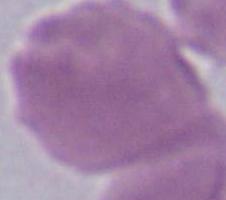

Summary:
  - Identification: erythrocyte
  - Magnification: 1000x
  - Modality: photomicrograph